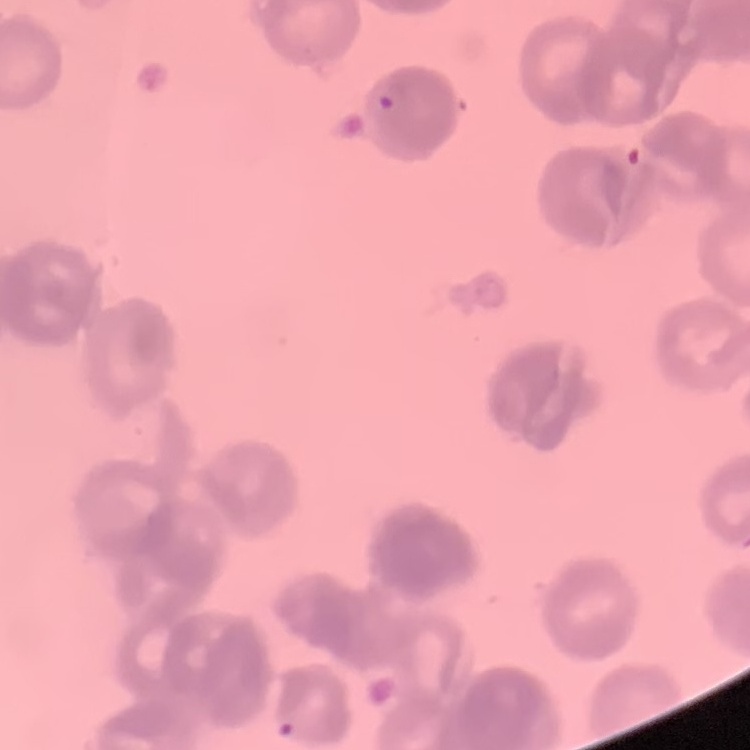

The erythrocytes show rouleaux formation. Thin blood smear. One tile cut from a larger photomicrograph. Stained with either Field's or Giemsa.